State which parasite is depicted.
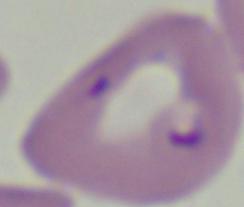

Babesia.

Summary:
  - Magnification: 1000x
  - Modality: photomicrograph